State which parasite is depicted.
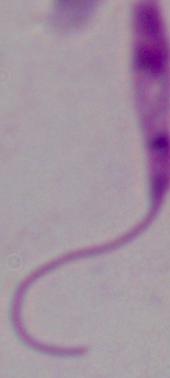

Leishmania.

1000x magnification. Micrograph.